Locate every blood parasite and identify its species.
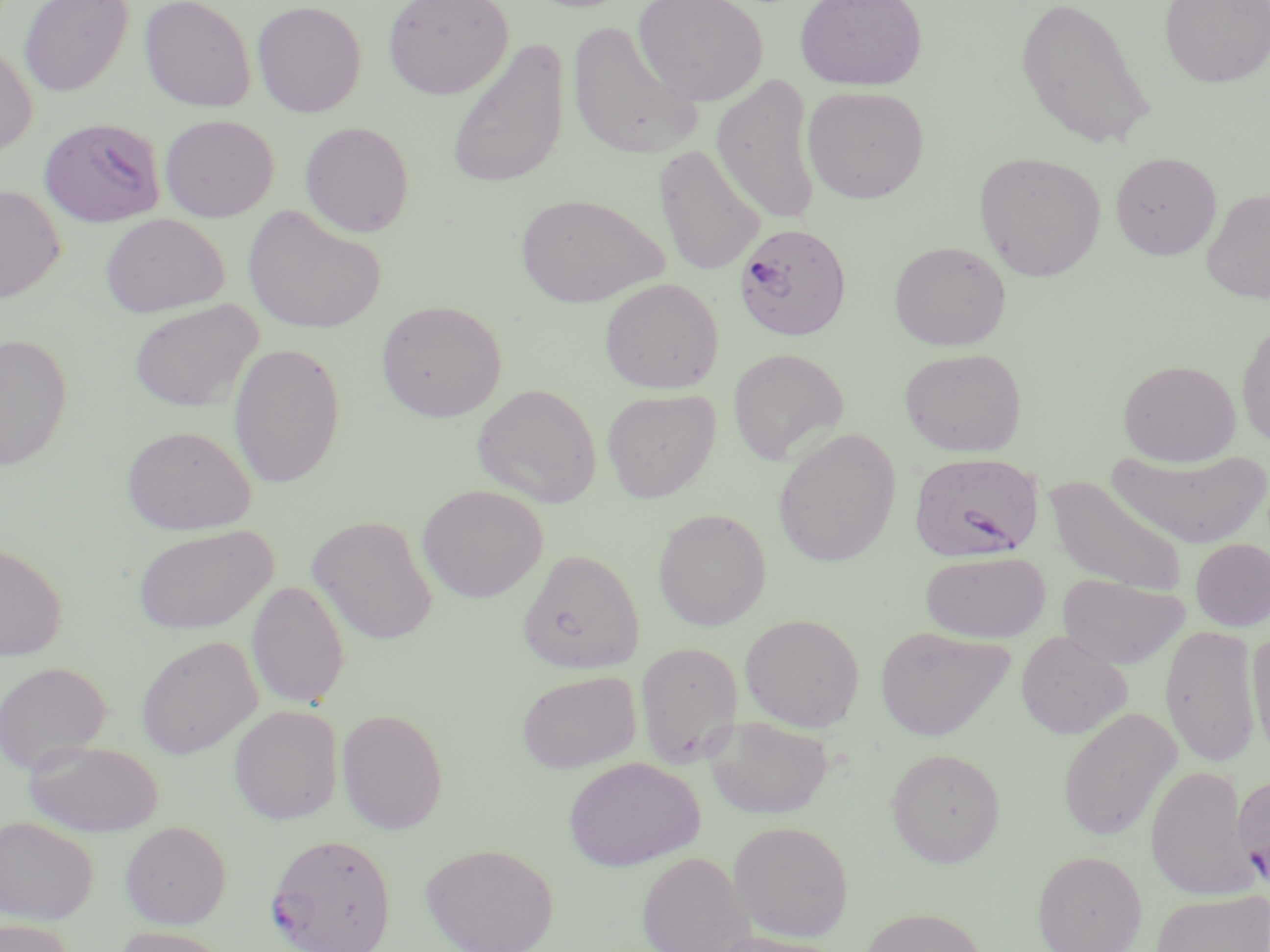
Approximate bounding boxes as named x1/y1/x2/y2 corners in pixels.
Plasmodium falciparum-infected red blood cells: (x1=39, y1=117, x2=165, y2=228), (x1=733, y1=222, x2=852, y2=342), (x1=908, y1=456, x2=1044, y2=566), (x1=1233, y1=772, x2=1270, y2=891), (x1=266, y1=833, x2=396, y2=952).
No Plasmodium ovale, Plasmodium malariae, Plasmodium vivax, Babesia divergens, or Trypanosoma brucei observed.

Summary:
  - Uninfected red blood cell locations: (x1=19, y1=0, x2=133, y2=96), (x1=139, y1=0, x2=256, y2=112), (x1=383, y1=0, x2=513, y2=100), (x1=632, y1=0, x2=769, y2=107), (x1=794, y1=0, x2=928, y2=91), (x1=1014, y1=0, x2=1159, y2=150), (x1=1159, y1=0, x2=1270, y2=88), (x1=252, y1=1, x2=367, y2=118), (x1=567, y1=21, x2=703, y2=160), (x1=447, y1=38, x2=571, y2=191), (x1=0, y1=44, x2=38, y2=157), (x1=710, y1=76, x2=822, y2=225), (x1=802, y1=85, x2=929, y2=203), (x1=159, y1=115, x2=279, y2=222), (x1=300, y1=121, x2=415, y2=237), (x1=653, y1=145, x2=766, y2=276), (x1=974, y1=151, x2=1107, y2=281), (x1=1110, y1=151, x2=1222, y2=260), (x1=0, y1=185, x2=66, y2=302), (x1=1201, y1=188, x2=1270, y2=303), (x1=515, y1=192, x2=668, y2=308), (x1=243, y1=206, x2=386, y2=335), (x1=100, y1=213, x2=229, y2=318), (x1=889, y1=241, x2=1011, y2=350), (x1=600, y1=277, x2=724, y2=393), (x1=128, y1=299, x2=264, y2=413), (x1=376, y1=300, x2=507, y2=422), (x1=1236, y1=321, x2=1270, y2=451), (x1=0, y1=332, x2=72, y2=472), (x1=228, y1=343, x2=345, y2=490), (x1=899, y1=347, x2=1027, y2=457), (x1=727, y1=348, x2=849, y2=466), (x1=1117, y1=359, x2=1241, y2=466), (x1=472, y1=383, x2=602, y2=508), (x1=602, y1=388, x2=721, y2=503), (x1=122, y1=424, x2=256, y2=535), (x1=772, y1=428, x2=901, y2=567), (x1=1109, y1=447, x2=1270, y2=549), (x1=1044, y1=474, x2=1188, y2=597), (x1=416, y1=484, x2=549, y2=603), (x1=653, y1=507, x2=771, y2=630), (x1=307, y1=515, x2=439, y2=645), (x1=132, y1=525, x2=277, y2=635), (x1=1190, y1=538, x2=1270, y2=631), (x1=0, y1=542, x2=67, y2=661), (x1=518, y1=549, x2=645, y2=675), (x1=920, y1=550, x2=1051, y2=643), (x1=1057, y1=574, x2=1189, y2=669), (x1=246, y1=580, x2=350, y2=709), (x1=739, y1=613, x2=865, y2=731), (x1=874, y1=625, x2=1014, y2=740), (x1=1160, y1=625, x2=1260, y2=768), (x1=1248, y1=630, x2=1270, y2=762), (x1=1015, y1=631, x2=1132, y2=739), (x1=136, y1=634, x2=262, y2=758), (x1=634, y1=641, x2=744, y2=768), (x1=0, y1=661, x2=112, y2=774), (x1=516, y1=669, x2=642, y2=773), (x1=228, y1=704, x2=343, y2=825), (x1=1058, y1=706, x2=1183, y2=842), (x1=336, y1=708, x2=449, y2=834), (x1=704, y1=715, x2=835, y2=819), (x1=25, y1=739, x2=164, y2=836), (x1=886, y1=747, x2=1006, y2=867), (x1=563, y1=756, x2=704, y2=871), (x1=1144, y1=765, x2=1257, y2=900), (x1=0, y1=816, x2=98, y2=925), (x1=728, y1=820, x2=855, y2=941), (x1=120, y1=821, x2=232, y2=929), (x1=420, y1=842, x2=559, y2=952), (x1=1033, y1=849, x2=1147, y2=952), (x1=637, y1=851, x2=756, y2=952), (x1=1152, y1=889, x2=1269, y2=952), (x1=859, y1=907, x2=990, y2=952), (x1=0, y1=918, x2=78, y2=952), (x1=109, y1=925, x2=237, y2=952), (x1=708, y1=933, x2=852, y2=952)
  - Slide-level diagnosis: Plasmodium falciparum
  - Stain: May-Grünwald-Giemsa
  - Image size: 1270×952 pixels
  - Modality: light microscopy
  - Preparation: thin blood smear
  - Field of view: one of a larger specimen
  - Magnification: 1000x